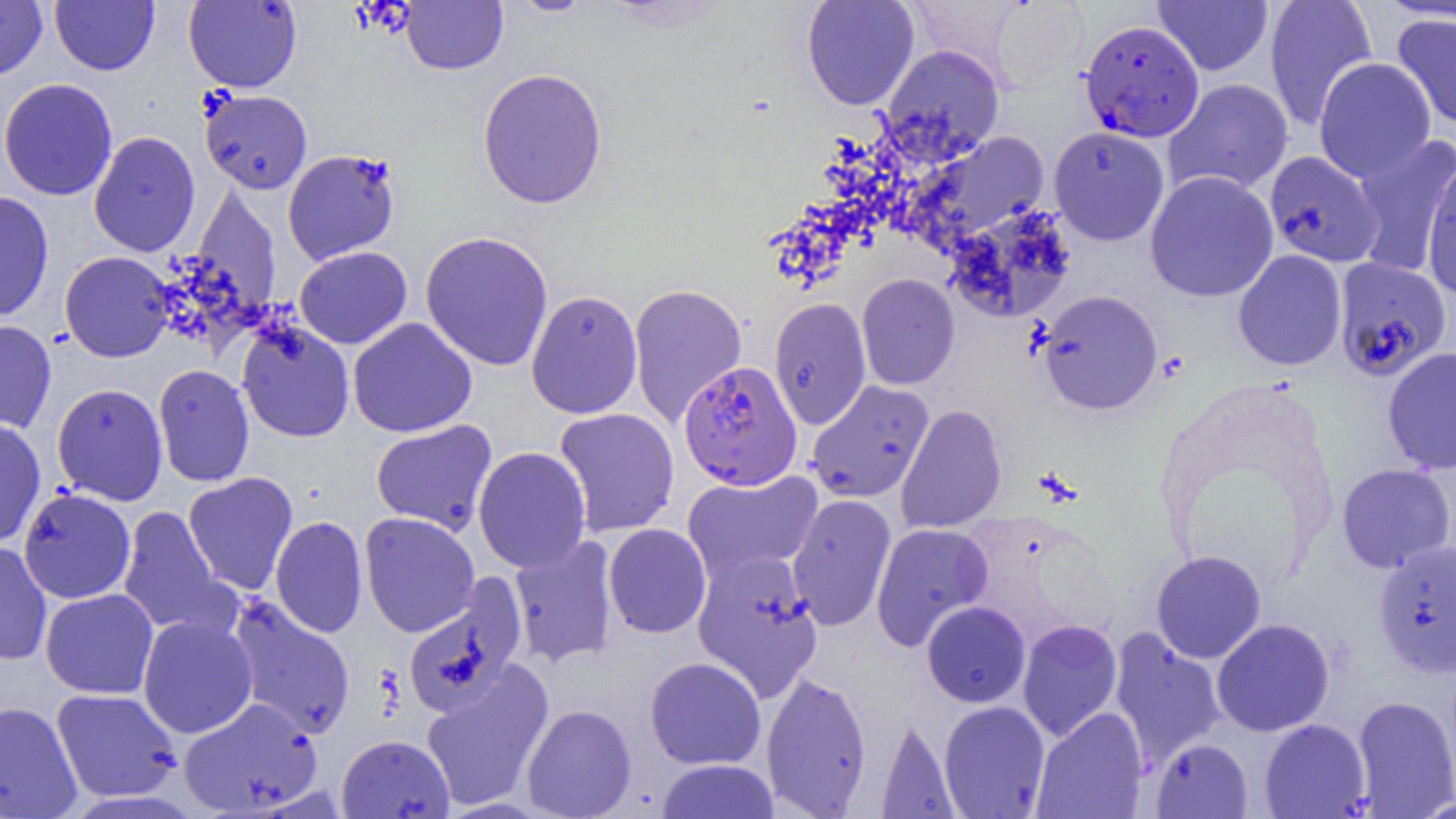

Summary:
  - Coordinate format: approximate bounding boxes as named x1/y1/x2/y2 corners in pixels
  - Plasmodium falciparum-infected red blood cell locations: (x1=1079, y1=19, x2=1204, y2=142), (x1=1332, y1=257, x2=1452, y2=382), (x1=679, y1=360, x2=803, y2=490)
  - Uninfected red blood cell locations: (x1=0, y1=0, x2=47, y2=80), (x1=183, y1=0, x2=302, y2=92), (x1=506, y1=0, x2=597, y2=17), (x1=801, y1=0, x2=919, y2=110), (x1=1264, y1=0, x2=1378, y2=131), (x1=51, y1=1, x2=159, y2=75), (x1=401, y1=1, x2=508, y2=74), (x1=990, y1=1, x2=1090, y2=90), (x1=1153, y1=1, x2=1273, y2=75), (x1=1391, y1=12, x2=1455, y2=130), (x1=880, y1=44, x2=1005, y2=162), (x1=1314, y1=57, x2=1436, y2=182), (x1=477, y1=67, x2=608, y2=209), (x1=0, y1=78, x2=118, y2=200), (x1=1163, y1=78, x2=1294, y2=197), (x1=200, y1=89, x2=312, y2=194), (x1=1048, y1=126, x2=1169, y2=245), (x1=88, y1=131, x2=200, y2=257), (x1=913, y1=131, x2=1050, y2=248), (x1=1350, y1=135, x2=1456, y2=278), (x1=283, y1=148, x2=401, y2=265), (x1=1264, y1=151, x2=1384, y2=268), (x1=1421, y1=159, x2=1456, y2=298), (x1=1144, y1=170, x2=1279, y2=302), (x1=191, y1=186, x2=282, y2=315), (x1=0, y1=191, x2=54, y2=323), (x1=945, y1=204, x2=1076, y2=322), (x1=420, y1=231, x2=554, y2=371), (x1=294, y1=246, x2=412, y2=349), (x1=1233, y1=250, x2=1347, y2=370), (x1=59, y1=251, x2=175, y2=362), (x1=857, y1=273, x2=960, y2=389), (x1=628, y1=283, x2=747, y2=427), (x1=526, y1=289, x2=643, y2=419), (x1=1037, y1=290, x2=1163, y2=415), (x1=769, y1=297, x2=871, y2=430), (x1=348, y1=317, x2=477, y2=438), (x1=0, y1=319, x2=56, y2=434), (x1=237, y1=321, x2=355, y2=442), (x1=1382, y1=347, x2=1456, y2=474), (x1=153, y1=364, x2=254, y2=487), (x1=806, y1=380, x2=934, y2=503), (x1=52, y1=383, x2=168, y2=505), (x1=896, y1=403, x2=1008, y2=534), (x1=553, y1=407, x2=680, y2=537), (x1=0, y1=417, x2=46, y2=547), (x1=371, y1=420, x2=497, y2=535), (x1=474, y1=446, x2=591, y2=574), (x1=1336, y1=462, x2=1456, y2=573), (x1=683, y1=470, x2=823, y2=584), (x1=183, y1=472, x2=298, y2=596), (x1=18, y1=488, x2=136, y2=604), (x1=786, y1=494, x2=897, y2=630), (x1=117, y1=506, x2=232, y2=637), (x1=359, y1=512, x2=479, y2=637), (x1=270, y1=515, x2=368, y2=638), (x1=870, y1=522, x2=994, y2=651), (x1=604, y1=523, x2=712, y2=638), (x1=509, y1=535, x2=619, y2=668), (x1=0, y1=540, x2=52, y2=666), (x1=1373, y1=540, x2=1456, y2=678), (x1=1150, y1=550, x2=1267, y2=664), (x1=692, y1=551, x2=823, y2=700), (x1=402, y1=575, x2=527, y2=718), (x1=41, y1=588, x2=158, y2=699), (x1=225, y1=596, x2=356, y2=739), (x1=921, y1=601, x2=1031, y2=707), (x1=138, y1=615, x2=258, y2=739), (x1=1211, y1=618, x2=1335, y2=737), (x1=1017, y1=619, x2=1123, y2=741), (x1=1109, y1=628, x2=1227, y2=769), (x1=644, y1=657, x2=767, y2=770), (x1=420, y1=661, x2=554, y2=811), (x1=761, y1=669, x2=872, y2=818), (x1=52, y1=688, x2=182, y2=803), (x1=1352, y1=694, x2=1456, y2=817), (x1=178, y1=696, x2=323, y2=816), (x1=938, y1=700, x2=1050, y2=818), (x1=0, y1=701, x2=83, y2=819), (x1=522, y1=703, x2=636, y2=818), (x1=1031, y1=707, x2=1148, y2=819), (x1=876, y1=715, x2=958, y2=819), (x1=1259, y1=718, x2=1371, y2=818), (x1=336, y1=734, x2=455, y2=818), (x1=1150, y1=738, x2=1253, y2=818), (x1=654, y1=759, x2=780, y2=818)
  - Slide-level diagnosis: Plasmodium falciparum
  - Image size: 1456×819 pixels
  - Field of view: one of a larger specimen
  - Modality: optical microscopy
  - Magnification: 1000x
  - Preparation: thin blood smear